Classify this cell by malaria status.
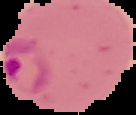
Parasitized.

preparation = thin blood film
image type = segmented cell region on a black background
image size = 136×115 pixels